Comment on the morphology of the erythrocytes.
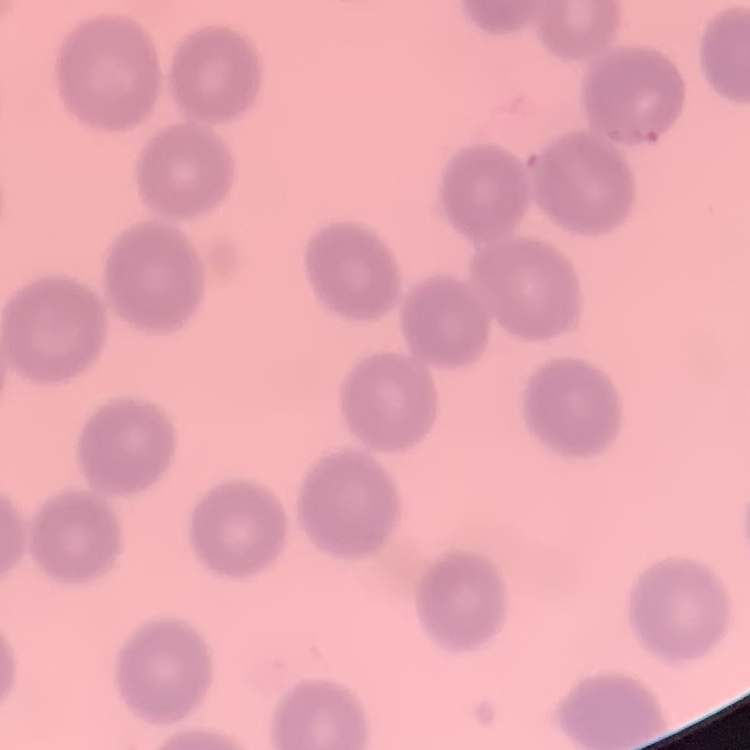
They show no rouleaux formation.

Square crop of a larger photomicrograph. Thin peripheral smear. Stained with either Field's or Giemsa.